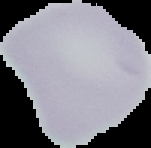

Summary:
  - Image size: 151×148 pixels
  - Result: no malaria parasites seen
  - Preparation: thin blood film
  - Image type: segmented cell region on a black background